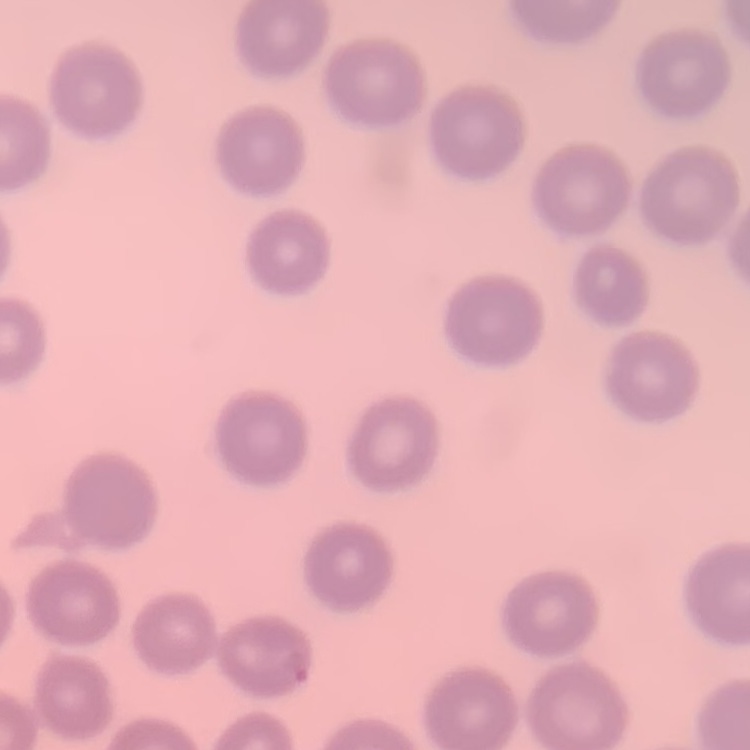

erythrocyte_morphology: no rouleaux formation
image_type: square crop of a larger photomicrograph
preparation: thin blood film
stain: Field's or Giemsa